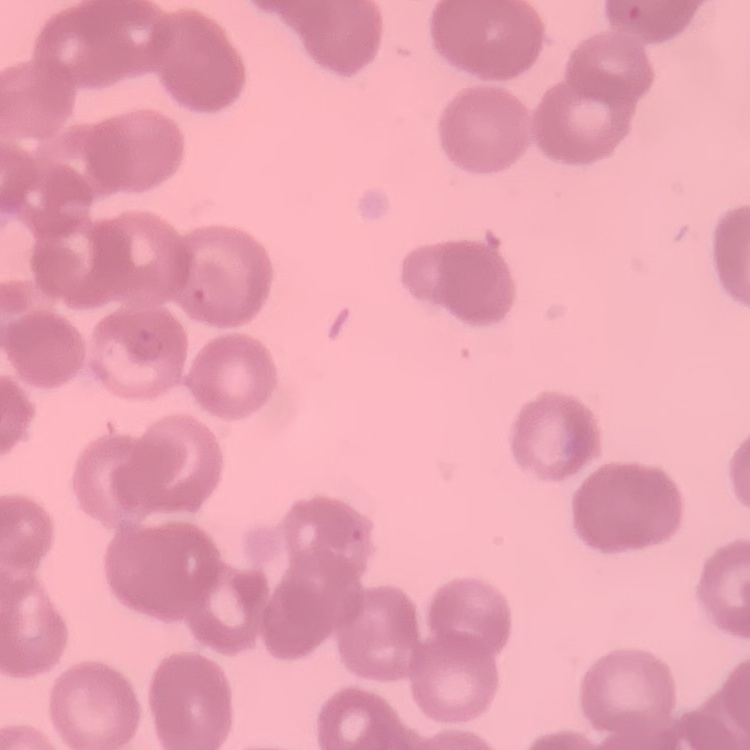

erythrocyte morphology = rouleaux formation
image type = square crop of a larger photomicrograph
preparation = thin peripheral smear
stain = Field's or Giemsa